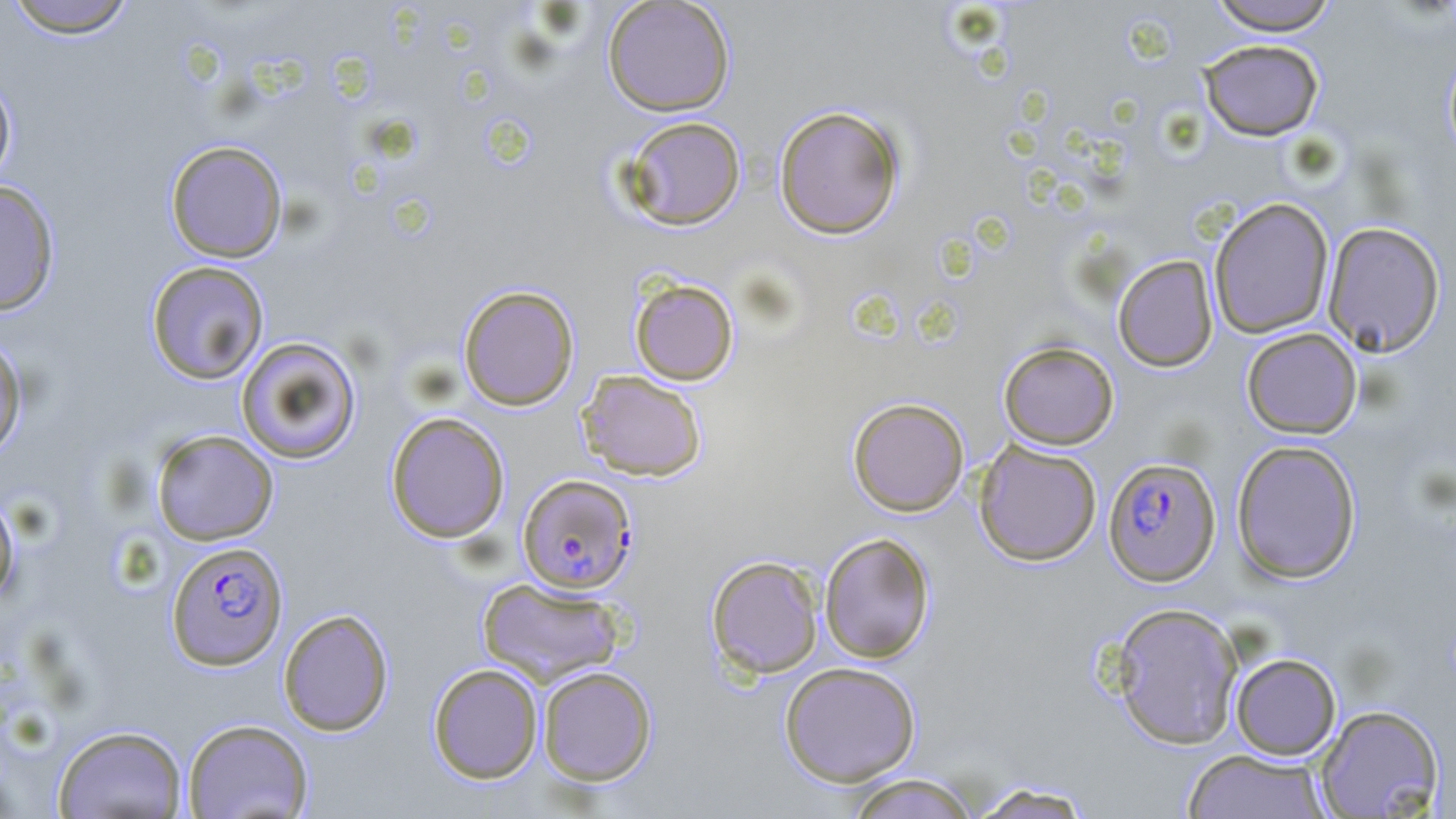
Approximate bounding boxes as (x1, y1, x2, y2) in pixels. Plasmodium falciparum-infected red blood cell locations: (1103, 457, 1221, 586), (517, 474, 638, 593), (166, 540, 288, 670). Uninfected red blood cell locations: (3, 0, 139, 38), (602, 0, 736, 116), (1206, 0, 1340, 35), (1198, 39, 1324, 141), (1443, 47, 1456, 161), (0, 70, 18, 190), (773, 104, 906, 239), (621, 116, 747, 231), (165, 140, 288, 263), (0, 180, 61, 316), (1209, 197, 1334, 339), (1322, 221, 1445, 357), (1113, 254, 1218, 372), (145, 260, 269, 385), (629, 277, 739, 386), (458, 284, 579, 411), (1242, 328, 1362, 438), (0, 332, 28, 461), (235, 336, 362, 465), (998, 340, 1119, 450), (577, 370, 708, 481), (848, 397, 970, 516), (386, 411, 510, 543), (151, 429, 279, 545), (974, 440, 1102, 566), (1231, 440, 1362, 584), (0, 486, 20, 610), (819, 532, 936, 663), (706, 555, 823, 679), (477, 577, 626, 686), (1109, 602, 1243, 749), (278, 608, 394, 736), (1230, 653, 1341, 760), (779, 661, 922, 786), (427, 663, 543, 783), (538, 666, 657, 785), (1315, 704, 1444, 817), (182, 718, 314, 818), (53, 724, 187, 819), (1182, 748, 1332, 819), (843, 773, 981, 819), (967, 781, 1097, 819). Slide-level diagnosis: Plasmodium falciparum. Thin blood film. Image is 1456×819 pixels. 1000x magnification. Single field of view. May-Grünwald-Giemsa-stained preparation. Optical microscopy.